State which cell type is depicted.
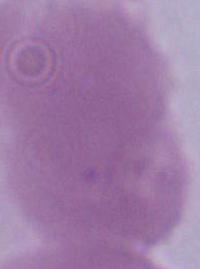
An erythrocyte.

Captured at 1000x magnification. Micrograph.